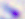 Toxoplasma gondii is seen. Captured at 400x magnification. Photomicrograph.